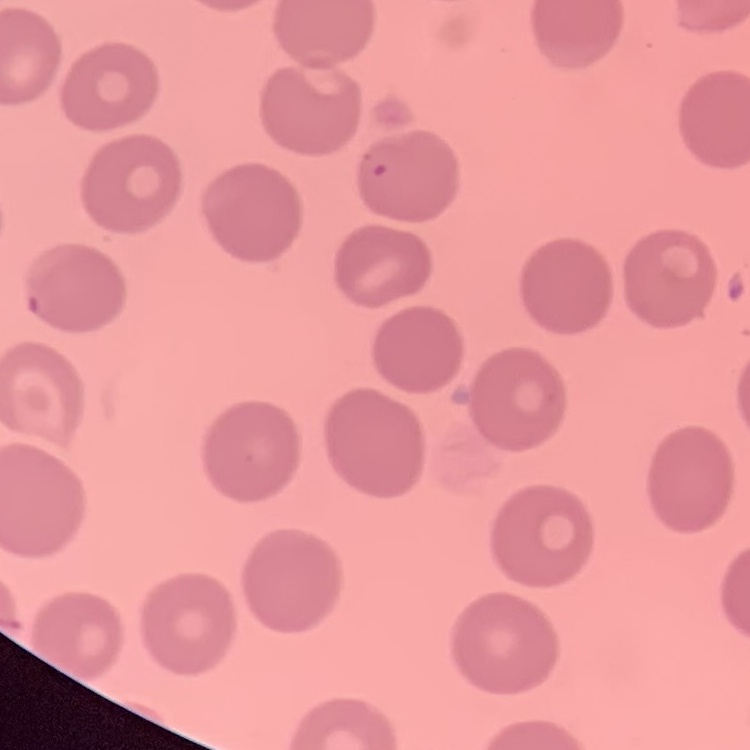

Summary:
  - Red blood cell morphology: no rouleaux formation
  - Preparation: thin blood smear
  - Image type: one tile cut from a larger photomicrograph
  - Stain: Field's or Giemsa